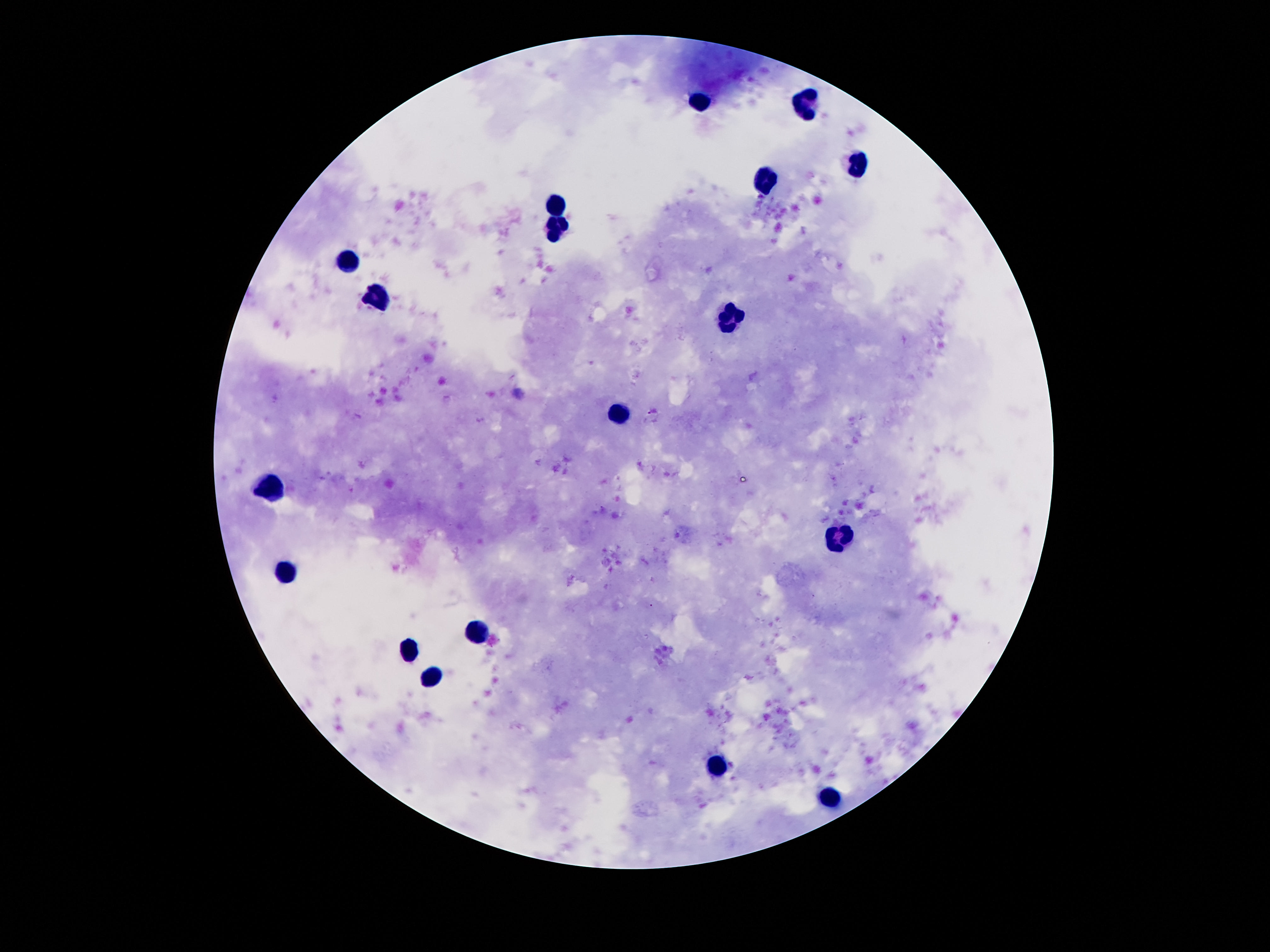

leukocyte locations = approximate centers as {x, y} in pixels: {698, 100}, {806, 100}, {858, 165}, {767, 180}, {554, 204}, {557, 226}, {349, 258}, {381, 298}, {732, 315}, {621, 412}, {270, 485}, {844, 538}, {285, 569}, {478, 629}, {411, 649}, {431, 676}, {717, 766}, {831, 799}
preparation = thick blood film
capture = smartphone camera through the microscope eyepiece
image size = 1270×952 pixels
field of view = one from this slide
stain = Giemsa
magnification = 100x
patient malaria status = not infected